State the blood parasite species.
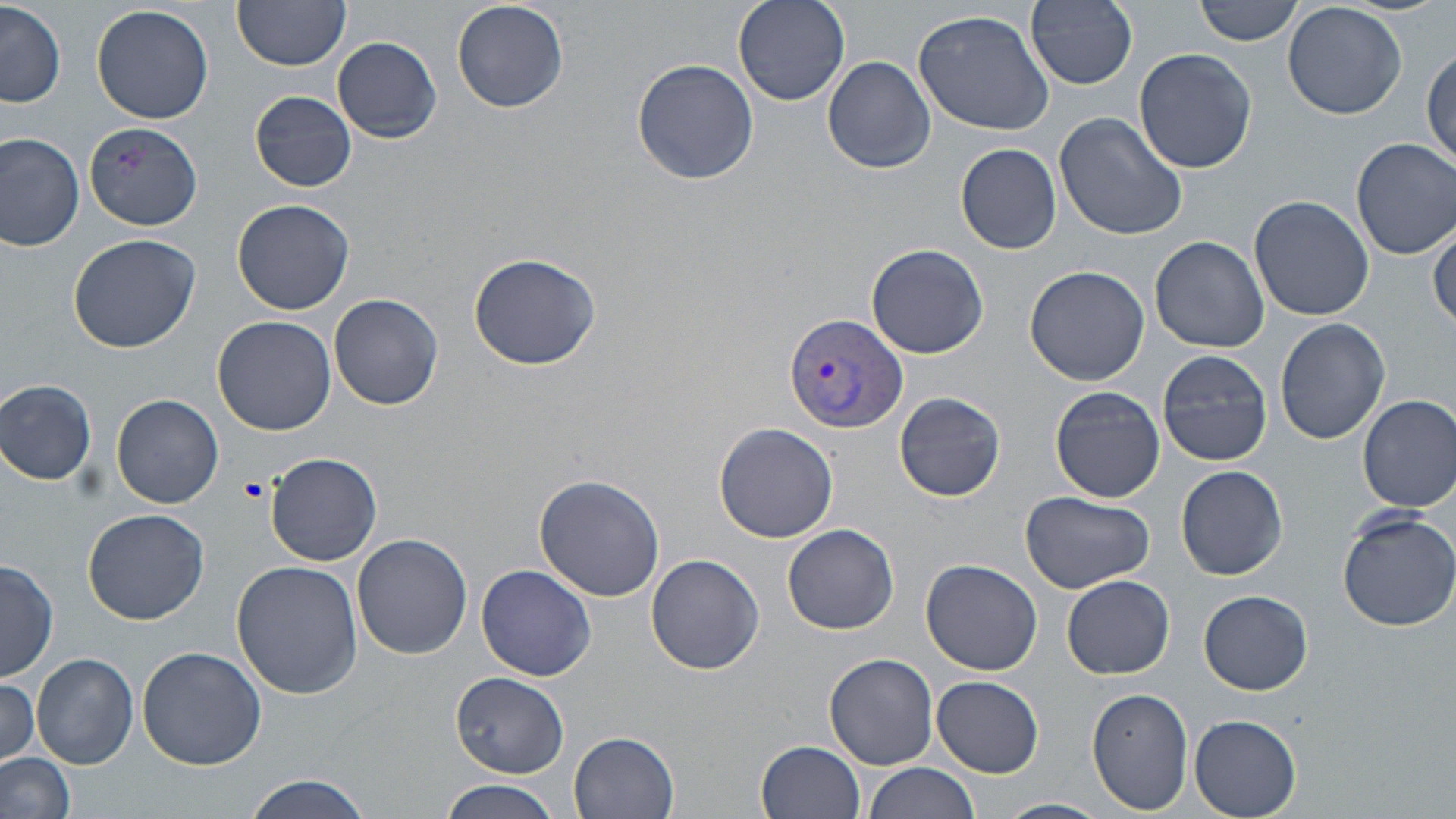
Plasmodium vivax.

Summary:
  - Coordinate format: approximate bounding boxes as (x1,y1)-(x2,y2) corner pairs in pixels
  - Platelet locations: (237,474)-(269,502)
  - Plasmodium vivax-infected red blood cell locations: (785,312)-(907,435)
  - Uninfected red blood cell locations: (231,0)-(350,71), (451,0)-(569,114), (734,0)-(850,105), (1028,0)-(1138,89), (1195,0)-(1303,45), (1283,1)-(1408,120), (1,3)-(66,108), (91,4)-(215,125), (912,9)-(1056,136), (334,38)-(441,141), (1426,44)-(1456,169), (1133,48)-(1257,174), (822,56)-(936,174), (632,57)-(758,185), (250,90)-(357,192), (1054,112)-(1188,241), (84,123)-(203,233), (0,135)-(84,250), (1353,138)-(1456,259), (956,143)-(1061,254), (1249,195)-(1375,321), (232,200)-(355,317), (1429,223)-(1456,330), (68,233)-(200,353), (1150,234)-(1268,352), (867,244)-(988,358), (468,251)-(601,371), (1024,265)-(1150,385), (330,293)-(443,410), (213,315)-(336,435), (1275,318)-(1391,446), (1157,350)-(1272,466), (0,378)-(98,486), (1049,387)-(1166,502), (891,390)-(1007,501), (112,393)-(225,509), (1357,394)-(1456,512), (713,422)-(838,542), (266,452)-(382,567), (1176,464)-(1288,580), (534,474)-(665,602), (1020,490)-(1156,594), (83,509)-(210,625), (1336,509)-(1456,632), (781,523)-(900,635), (353,534)-(472,660), (646,554)-(764,676), (1,558)-(57,680), (920,559)-(1043,677), (232,561)-(363,698), (476,563)-(597,680), (1062,575)-(1174,679), (1200,588)-(1312,695), (138,645)-(267,769), (824,653)-(940,769), (32,654)-(138,767), (451,671)-(568,778), (0,675)-(41,768), (931,675)-(1044,777), (1086,686)-(1194,815), (1188,713)-(1302,818), (570,732)-(678,817), (756,739)-(863,817), (0,751)-(75,819), (865,761)-(980,819), (241,775)-(373,818), (440,781)-(560,819), (994,797)-(1109,819)
  - Modality: light microscopy
  - Stain: May-Grünwald-Giemsa
  - Preparation: thin blood smear
  - Image size: 1456×819 pixels
  - Field of view: one of a larger specimen
  - Magnification: 1000x